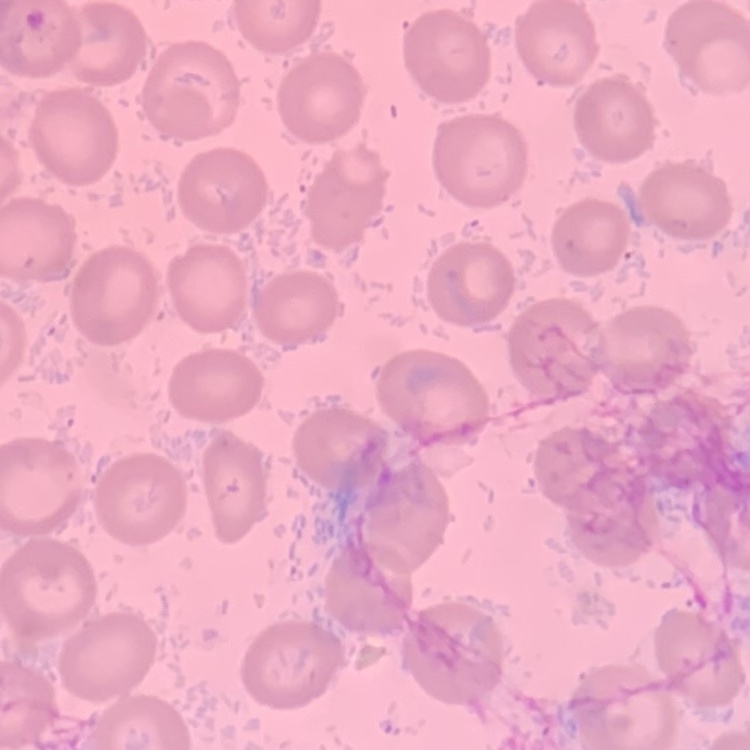

erythrocyte morphology = no rouleaux formation
stain = Field's or Giemsa
image type = square crop of a larger photomicrograph
preparation = thin peripheral smear